Comment on the morphology of the erythrocytes.
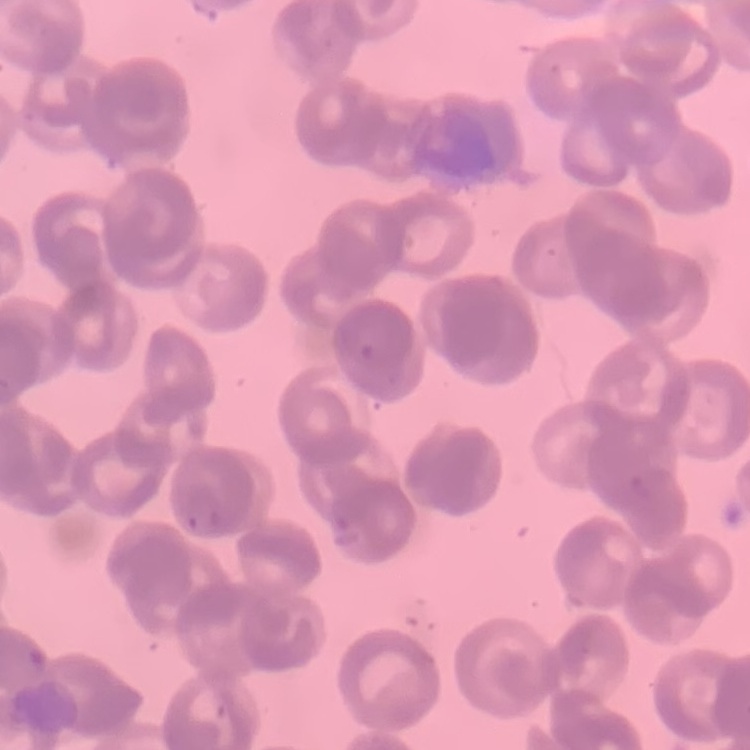
They show rouleaux formation.

Summary:
  - Image type: square crop of a larger photomicrograph
  - Stain: Field's or Giemsa
  - Preparation: thin peripheral smear